Classify this cell by malaria status.
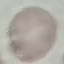
It is uninfected.

Summary:
  - Stain: Giemsa
  - Capture: smartphone camera at the microscope eyepiece
  - Image type: automatically extracted cell patch, resized to 64 × 64 pixels
  - Preparation: thin blood film